Locate every leukocyte (white blood cell).
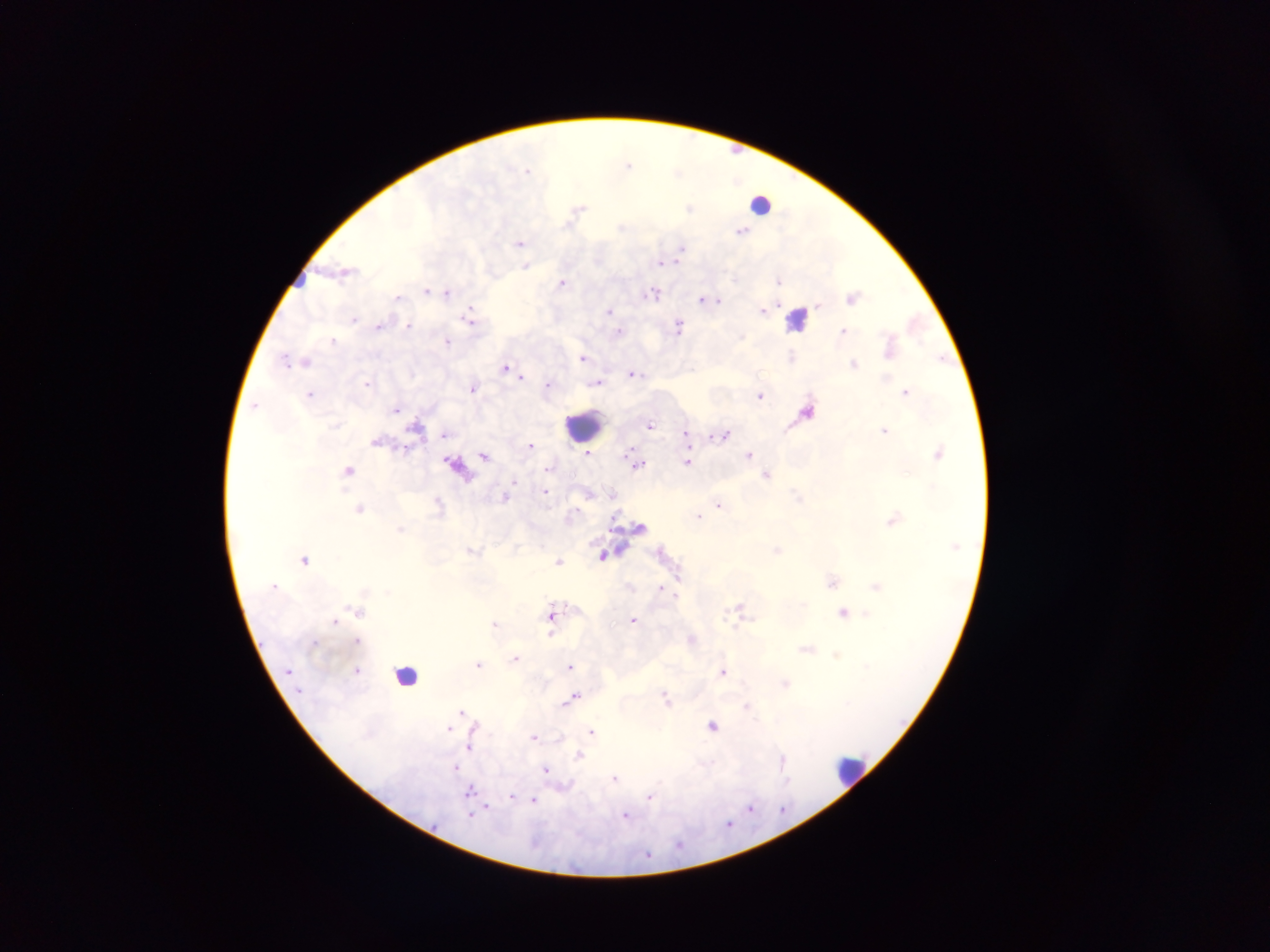

Approximate centers as [x, y] in pixels.
Leukocytes: [797, 319], [585, 426], [407, 676], [849, 770].

field of view = single
capture = mobile-phone photograph through a microscope
image size = 1270×952 pixels
country = Ghana
preparation = thick blood smear
malaria parasite locations = approximate centers as [x, y] in pixels: [629, 164], [527, 170], [679, 171], [760, 202], [690, 207], [579, 211], [622, 226], [742, 230], [520, 242], [682, 249], [661, 262], [525, 266], [735, 278], [779, 280], [562, 282], [427, 290], [447, 291], [654, 294], [398, 297], [854, 297], [701, 298], [709, 299], [719, 300], [819, 305], [763, 310], [609, 311], [469, 317], [353, 318], [380, 326], [408, 326], [679, 326], [843, 330], [619, 331], [333, 340], [447, 341], [285, 358], [583, 358], [791, 358], [943, 358], [307, 361], [854, 363], [505, 367], [633, 373], [521, 376], [598, 381], [367, 382], [549, 385], [474, 387], [905, 391], [310, 394], [760, 396], [255, 405], [396, 410], [807, 410], [418, 423], [650, 424], [885, 430], [445, 434], [725, 434], [686, 435], [715, 436], [531, 445], [939, 452], [587, 453], [628, 453], [485, 455], [750, 455], [689, 462], [454, 463], [638, 464], [549, 468], [348, 470], [768, 474], [514, 481], [547, 491], [798, 495], [506, 496], [439, 502], [719, 505], [360, 508], [699, 516], [893, 520], [640, 526], [400, 528], [777, 550], [473, 551], [662, 551], [603, 554], [305, 559], [558, 561], [678, 578], [832, 582], [876, 585], [660, 587], [740, 607], [357, 610], [843, 613], [865, 614], [551, 615], [634, 620], [335, 621], [494, 623], [550, 634], [692, 638], [357, 640], [315, 642], [807, 649], [836, 655], [516, 657], [478, 664], [570, 666], [867, 666], [357, 670], [723, 671], [785, 683], [666, 697], [573, 698], [747, 706], [462, 710], [476, 724], [712, 727], [448, 728], [592, 732], [534, 736], [470, 748], [579, 755], [782, 757], [710, 763], [456, 767], [547, 769], [615, 778], [788, 781], [470, 790], [650, 796], [511, 798], [534, 800], [487, 807], [751, 807], [783, 809], [470, 814], [625, 814], [729, 823], [679, 846], [648, 854]